Give the preparation type.
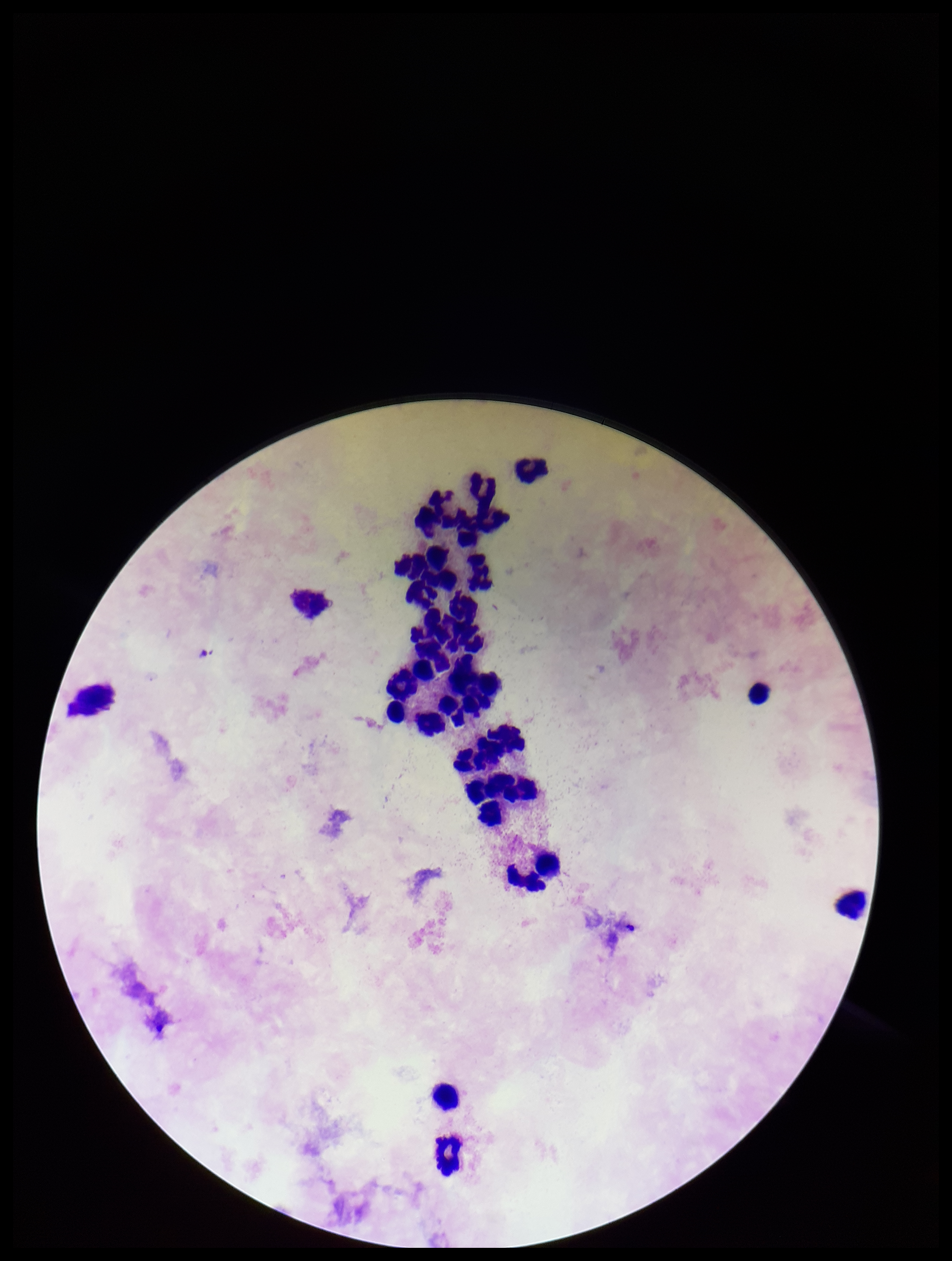

Thick.

{
  "leukocyte_count": 21,
  "field_of_view": "one from this slide",
  "stain": "Giemsa",
  "image_size": "952×1261 pixels",
  "parasite_count": 0,
  "capture": "smartphone photograph through the microscope eyepiece",
  "plasmodium_parasites": "none identified",
  "patient_malaria_status": "negative"
}